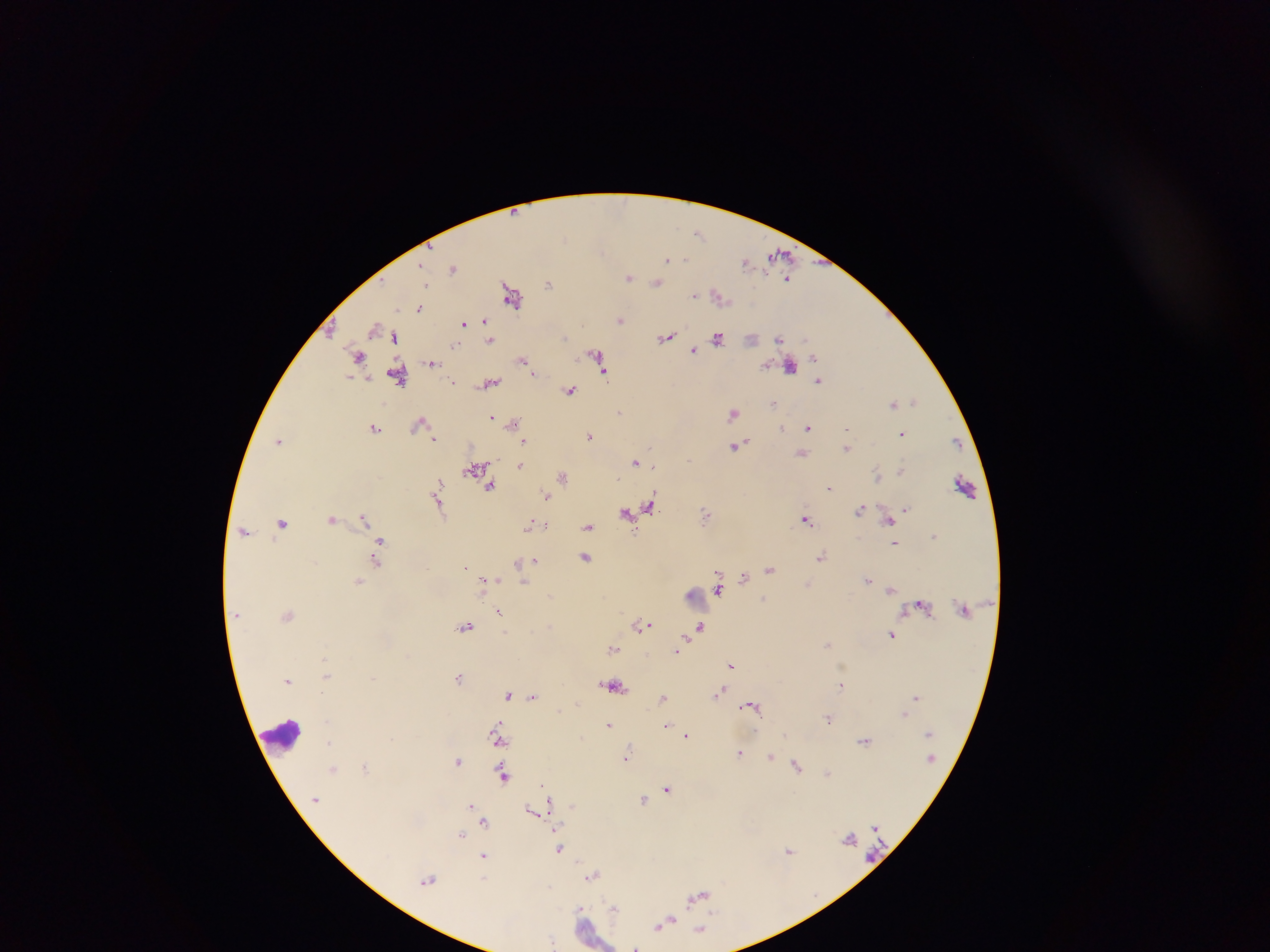 Approximate centers as {x, y} in pixels. Leukocyte locations (subset; some below the resolvable size): {966, 487}, {696, 596}, {281, 733}. Plasmodium parasite locations: {699, 233}, {564, 238}, {780, 255}, {667, 258}, {683, 259}, {746, 262}, {453, 269}, {629, 276}, {788, 279}, {549, 283}, {657, 283}, {511, 294}, {695, 295}, {719, 296}, {420, 308}, {620, 320}, {463, 322}, {485, 322}, {375, 327}, {487, 333}, {666, 336}, {564, 337}, {395, 338}, {718, 338}, {778, 338}, {490, 339}, {752, 339}, {456, 345}, {694, 350}, {358, 355}, {598, 357}, {814, 357}, {522, 360}, {432, 363}, {601, 366}, {789, 366}, {605, 373}, {397, 374}, {533, 374}, {819, 380}, {453, 383}, {490, 383}, {569, 390}, {914, 400}, {893, 403}, {772, 404}, {619, 413}, {733, 414}, {491, 416}, {421, 422}, {513, 424}, {809, 427}, {374, 428}, {781, 428}, {848, 430}, {902, 433}, {589, 435}, {435, 439}, {279, 440}, {523, 440}, {737, 445}, {848, 448}, {802, 453}, {690, 459}, {636, 461}, {520, 465}, {653, 466}, {475, 469}, {901, 471}, {878, 476}, {562, 477}, {491, 487}, {829, 488}, {438, 492}, {547, 496}, {438, 501}, {650, 506}, {906, 508}, {860, 509}, {627, 514}, {706, 515}, {364, 518}, {331, 519}, {806, 520}, {889, 521}, {282, 522}, {530, 525}, {545, 526}, {588, 527}, {245, 531}, {934, 536}, {895, 543}, {379, 545}, {822, 556}, {586, 558}, {376, 561}, {536, 561}, {518, 562}, {466, 567}, {769, 569}, {744, 576}, {868, 580}, {358, 581}, {484, 582}, {523, 584}, {719, 588}, {891, 590}, {764, 598}, {920, 605}, {500, 612}, {288, 615}, {643, 625}, {466, 626}, {700, 627}, {892, 634}, {828, 644}, {613, 649}, {677, 651}, {732, 665}, {327, 676}, {459, 678}, {288, 680}, {615, 685}, {841, 685}, {322, 692}, {720, 692}, {508, 694}, {533, 696}, {663, 697}, {916, 697}, {750, 706}, {903, 715}, {828, 718}, {610, 724}, {667, 725}, {785, 734}, {687, 736}, {497, 737}, {864, 741}, {329, 743}, {740, 753}, {627, 757}, {771, 758}, {458, 761}, {365, 766}, {796, 766}, {334, 769}, {827, 773}, {504, 775}, {543, 786}, {668, 788}, {643, 799}, {550, 800}, {472, 805}, {534, 811}, {484, 823}, {461, 835}, {849, 838}, {560, 848}, {788, 851}, {484, 856}, {593, 876}, {428, 880}, {699, 895}, {614, 908}, {581, 913}, {665, 923}, {701, 930}, {553, 942}, {636, 946}. Thick blood smear. Image is 1270×952 pixels. Photographed through a microscope with a mobile-phone camera. Collected in Ghana. Single field of view.